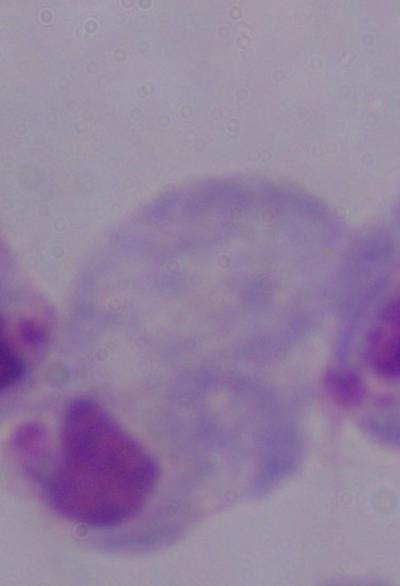
Summary:
  - Identification: trichomonad
  - Modality: photomicrograph
  - Magnification: 1000x